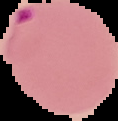

From a thin blood smear. Malaria status: parasitized. Image is 118×121 pixels. Segmented cell region on a black background.